Report the malaria status of this cell.
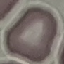
It is uninfected.

Summary:
  - Preparation: thin blood smear
  - Capture: smartphone camera at the microscope eyepiece
  - Image type: automatically extracted cell patch, resized to 64 × 64 pixels
  - Stain: Giemsa